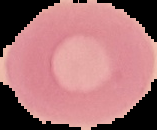
Summary:
  - Image type: segmented cell region with the area outside set to black
  - Result: no Plasmodium parasites seen
  - Image size: 157×130 pixels
  - Preparation: thin blood smear